Classify this cell by malaria status.
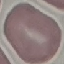
Uninfected.

Automatically extracted cell patch, resized to 64 × 64 pixels. Thin blood film. Giemsa-stained preparation. Photographed with a smartphone camera at the microscope eyepiece.